Name the cell type shown.
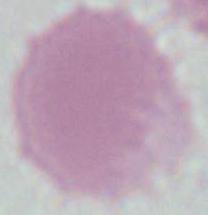

This is an erythrocyte.

Summary:
  - Magnification: 1000x
  - Modality: micrograph